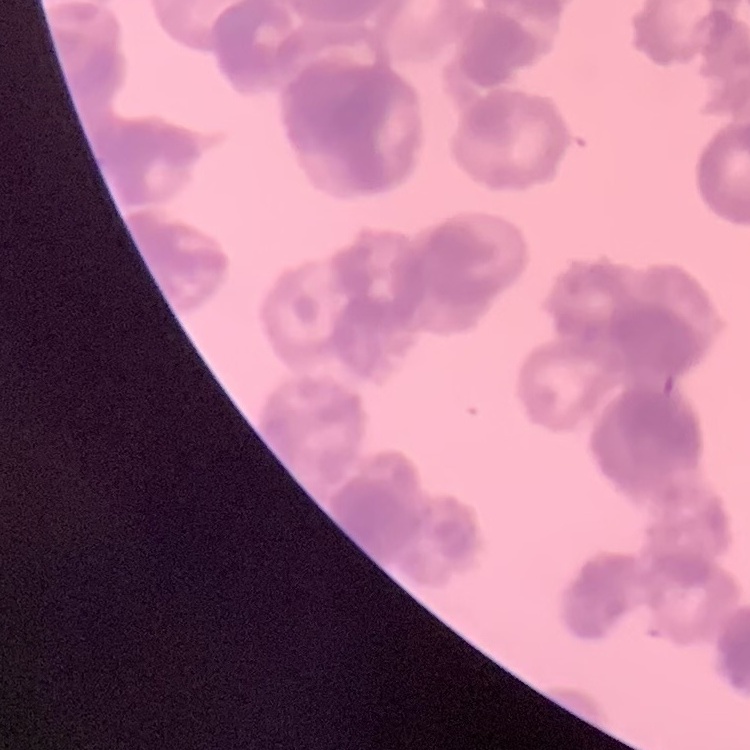
The red blood cells show rouleaux formation. Thin blood film. One tile cut from a larger photomicrograph. Stained with either Field's or Giemsa.